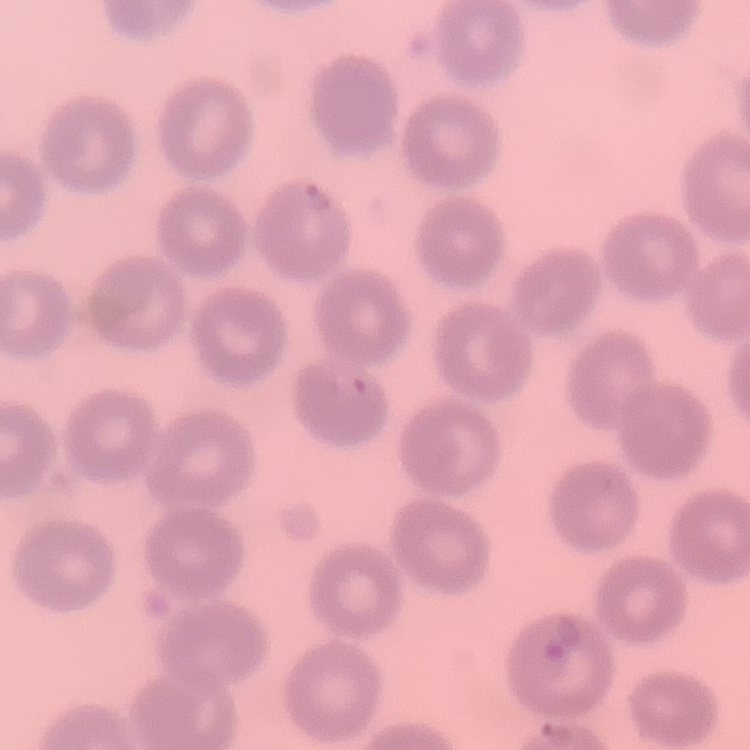 The erythrocytes show no rouleaux formation. One tile cut from a larger photomicrograph. Stained with either Field's or Giemsa. Thin blood film.